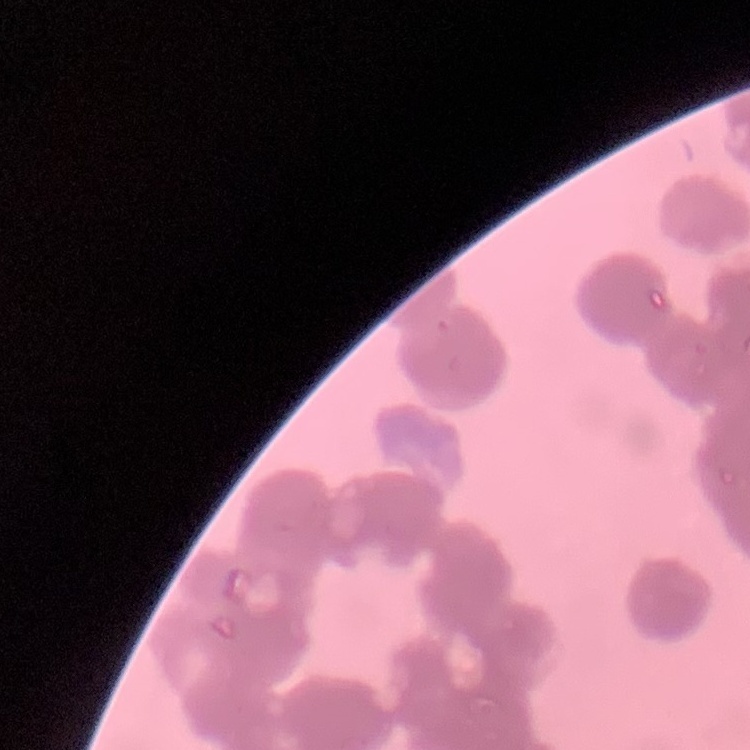
The erythrocytes exhibit rouleaux formation. Field's or Giemsa stain. Thin peripheral smear. Square crop of a larger photomicrograph.